Give the extent of all Plasmodium falciparum-infected red blood cells.
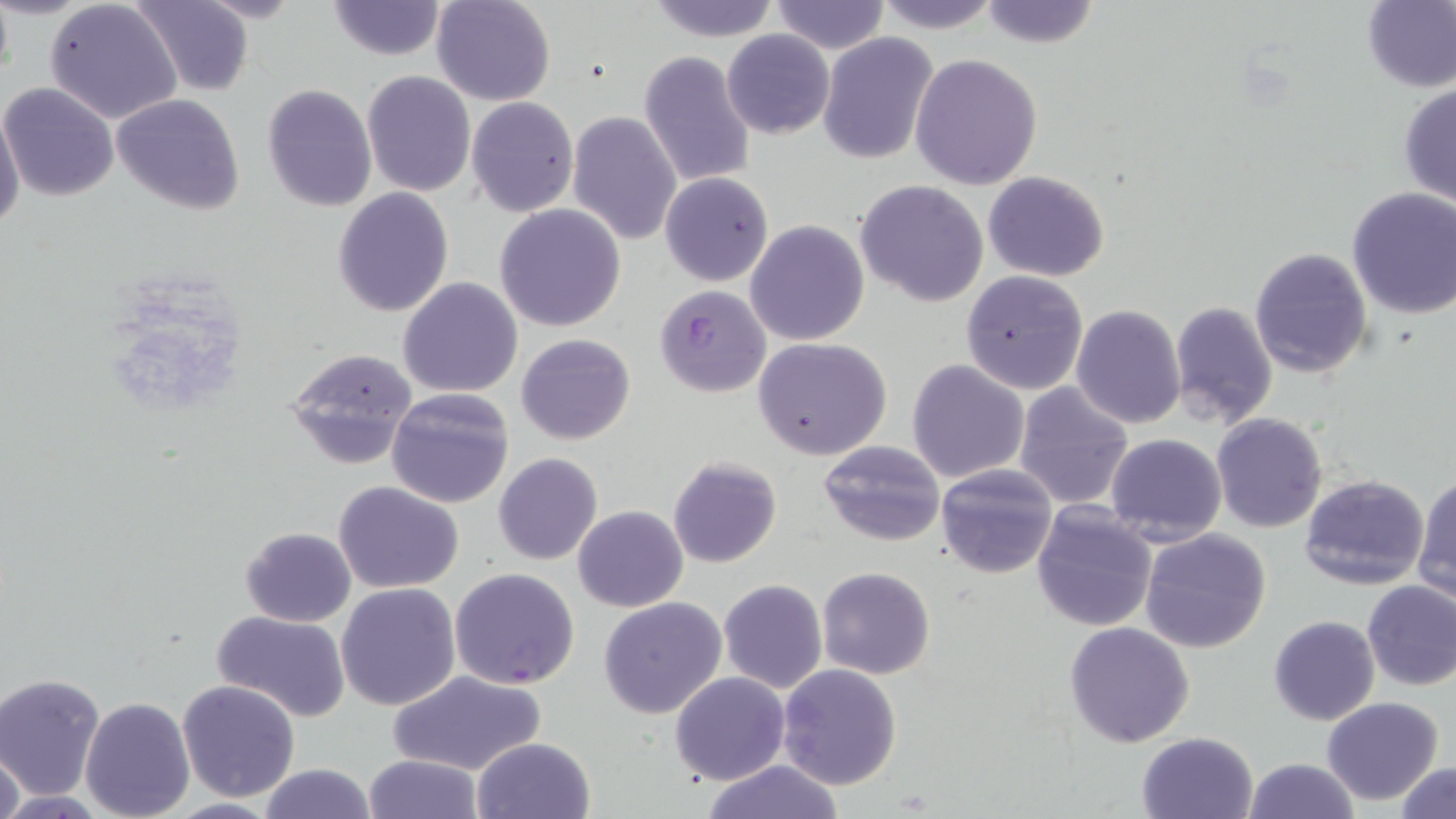
Approximate bounding boxes as (x1,y1)-(x2,y2) corner pairs in pixels.
Plasmodium falciparum-infected red blood cells: (655,285)-(772,397).

slide-level diagnosis = Plasmodium falciparum
field of view = single
magnification = 1000x
preparation = thin blood film
image size = 1456×819 pixels
uninfected red blood cell locations = approximate bounding boxes as (x1,y1)-(x2,y2) corner pairs in pixels: (131,0)-(256,95), (326,0)-(447,59), (431,0)-(556,106), (643,0)-(783,42), (875,0)-(1001,31), (976,0)-(1100,49), (1360,0)-(1456,92), (45,1)-(183,124), (769,1)-(890,54), (722,29)-(834,138), (818,32)-(939,165), (638,51)-(758,191), (910,54)-(1043,191), (361,71)-(476,197), (0,82)-(118,201), (1398,83)-(1455,207), (261,84)-(377,212), (112,94)-(244,215), (465,97)-(579,218), (0,105)-(26,238), (568,109)-(683,247), (983,170)-(1109,280), (660,172)-(774,285), (856,180)-(988,306), (1346,187)-(1456,320), (331,188)-(453,317), (494,202)-(626,332), (745,219)-(869,347), (1249,245)-(1374,379), (960,269)-(1089,394), (397,277)-(523,399), (1169,300)-(1279,428), (1071,303)-(1186,429), (516,333)-(636,445), (753,338)-(894,460), (282,347)-(418,470), (907,359)-(1031,483), (1012,382)-(1134,509), (385,386)-(515,510), (1211,412)-(1327,534), (1105,434)-(1228,546), (817,439)-(945,547), (494,452)-(603,566), (666,456)-(781,569), (936,464)-(1058,578), (1300,473)-(1431,592), (1412,474)-(1456,602), (332,480)-(465,595), (1031,501)-(1159,632), (572,505)-(688,612), (240,526)-(357,626), (1140,527)-(1272,654), (449,567)-(580,690), (816,567)-(937,679), (718,579)-(828,692), (1362,580)-(1456,691), (336,584)-(461,710), (597,597)-(728,719), (208,611)-(353,723), (1268,615)-(1380,725), (1064,622)-(1194,748), (777,664)-(904,791), (387,668)-(546,777), (670,672)-(791,787), (1,673)-(105,799), (176,679)-(301,802), (80,696)-(196,819), (1321,697)-(1444,805), (1136,732)-(1260,819), (471,737)-(596,819), (0,739)-(26,819), (363,752)-(483,819), (1243,758)-(1360,818), (700,760)-(847,817), (1393,762)-(1456,818), (256,764)-(377,819)
modality = optical microscopy
stain = May-Grünwald-Giemsa